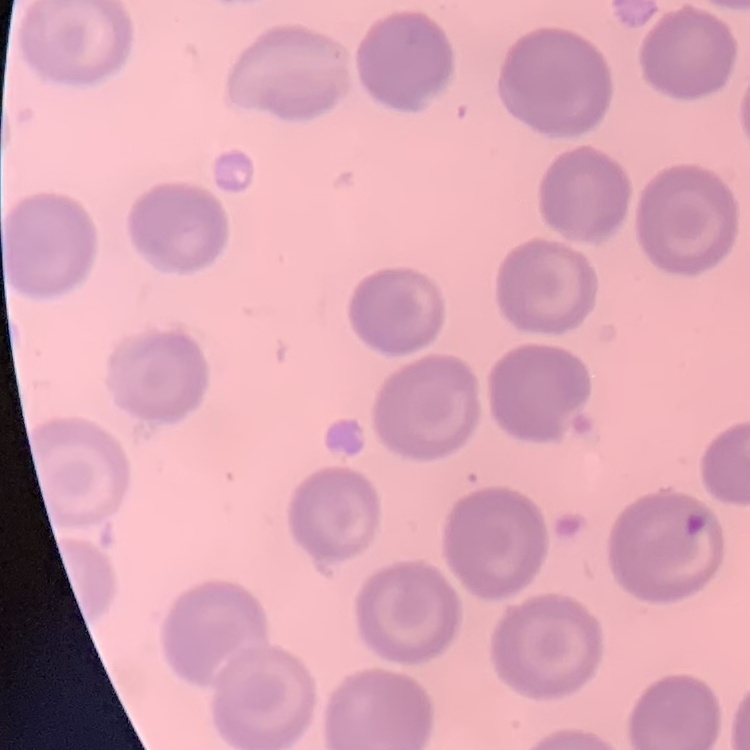
The red blood cells show no rouleaux formation. Stained with either Field's or Giemsa. Thin blood film. One tile cut from a larger photomicrograph.